State which parasite is depicted.
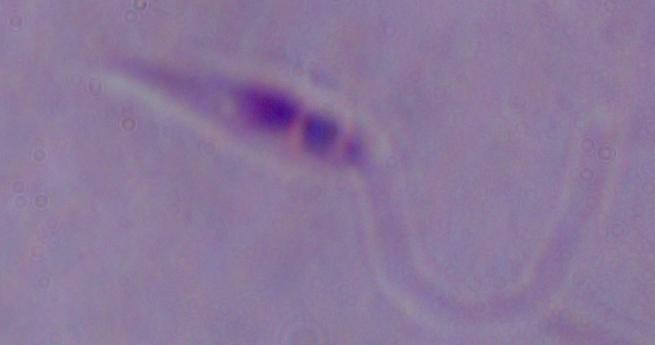
Leishmania.

Summary:
  - Magnification: 1000x
  - Modality: micrograph